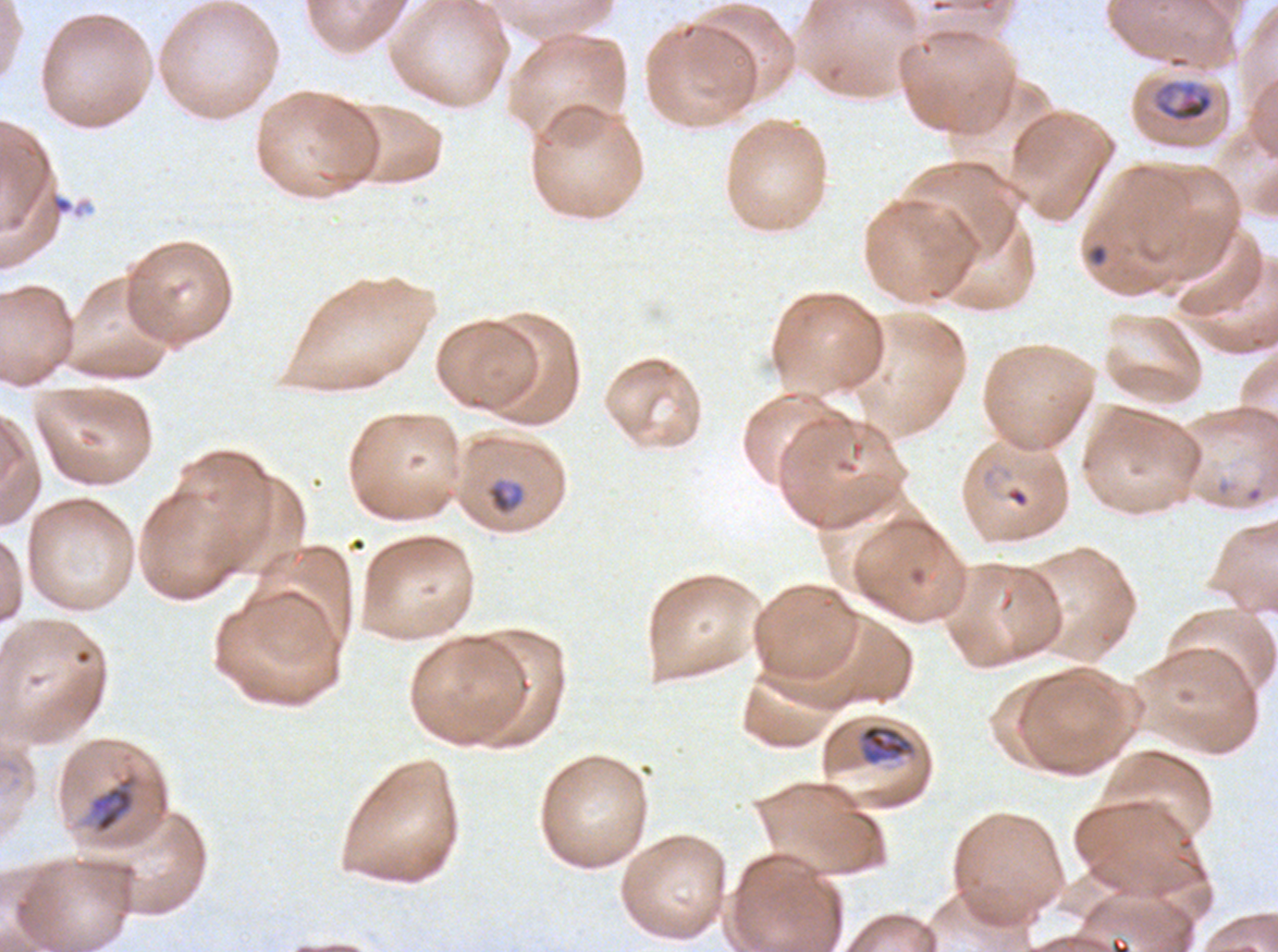

{
  "field_of_view": "sub-image separated from a larger composite",
  "late_ring_early_trophozoite_locations": "approximate bounding rectangles given as corner coordinates in pixels from the top-left: (x1=485, y1=479, x2=525, y2=516), (x1=1006, y1=488, x2=1028, y2=507)",
  "specimen": "Plasmodium falciparum from a patient in The Gambia, cultured ex vivo for 24 to 48 hours",
  "mid_trophozoite_locations": "approximate bounding rectangles given as corner coordinates in pixels from the top-left: (x1=1154, y1=79, x2=1214, y2=124), (x1=858, y1=724, x2=915, y2=765), (x1=86, y1=770, x2=141, y2=836)",
  "stain": "Giemsa",
  "preparation": "thin blood film",
  "debris_locations": "approximate bounding rectangles given as corner coordinates in pixels from the top-left: (x1=52, y1=196, x2=73, y2=214)",
  "life_cycle_stages_observed": "late-ring/early-trophozoite, mid trophozoite",
  "image_size": "1278×952 pixels"
}